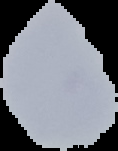 Image is 118×151 pixels. The area outside the segmented cell region is set to black. Malaria status: uninfected. From a thin blood film.